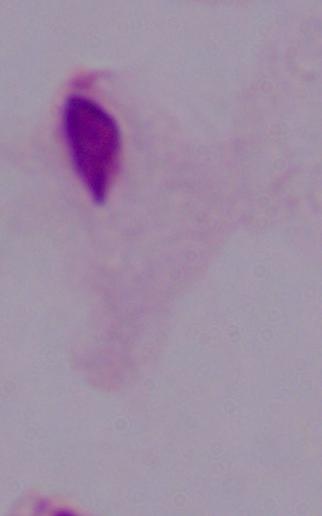
{
  "modality": "photomicrograph",
  "identification": "trichomonad",
  "magnification": "1000x"
}